State which parasite is depicted.
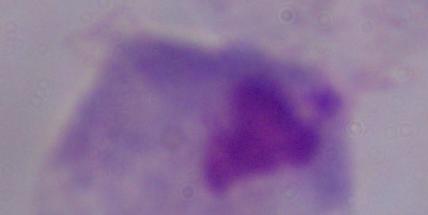
This is a trichomonad.

magnification = 1000x
modality = micrograph